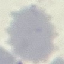
Malaria status: uninfected. Giemsa-stained preparation. Acquired by smartphone through the microscope eyepiece. Thin blood smear. Automatically extracted cell patch, resized to 64 × 64 pixels.